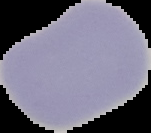
Summary:
  - Preparation: thin blood smear
  - Result: no Plasmodium parasites detected
  - Image type: segmented cell region with the area outside set to black
  - Image size: 151×133 pixels